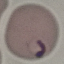

Summary:
  - Malaria status: parasitized
  - Capture: smartphone camera at the microscope eyepiece
  - Preparation: thin smear
  - Image type: automatically extracted cell patch, resized to 64 × 64 pixels
  - Stain: Giemsa